Assess this cell for malaria.
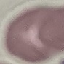

It is uninfected.

Thin blood smear. Giemsa-stained preparation. Photographed with a smartphone camera at the microscope eyepiece. Automatically extracted cell patch, resized to 64 × 64 pixels.